State which cell type is depicted.
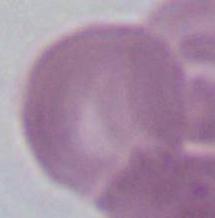

An erythrocyte.

Summary:
  - Magnification: 1000x
  - Modality: photomicrograph